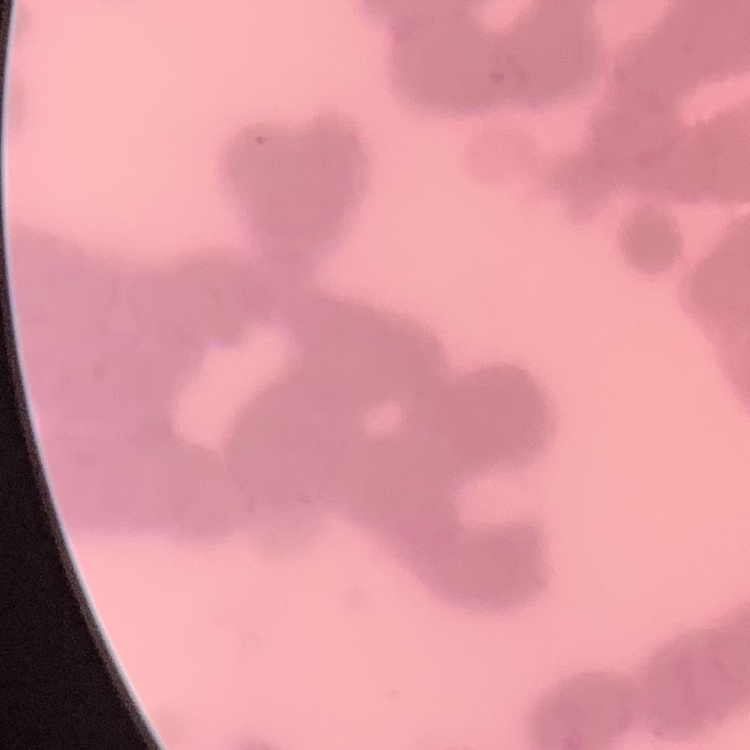
Summary:
  - Red blood cell morphology: rouleaux formation
  - Stain: Field's or Giemsa
  - Image type: square crop of a larger photomicrograph
  - Preparation: thin blood film